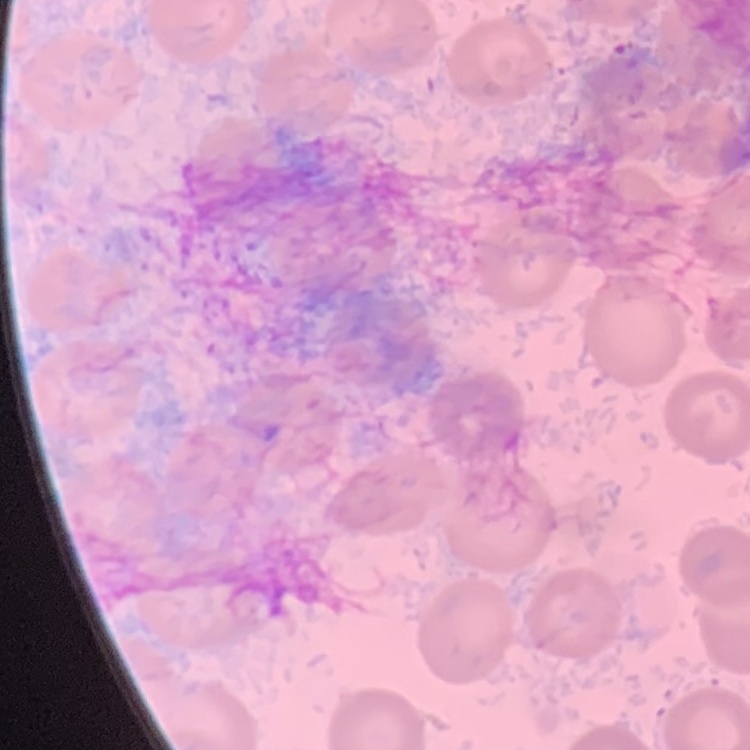

The red blood cells show no rouleaux formation. Stained with either Field's or Giemsa. Thin blood smear. Square crop of a larger photomicrograph.